Report the malaria status.
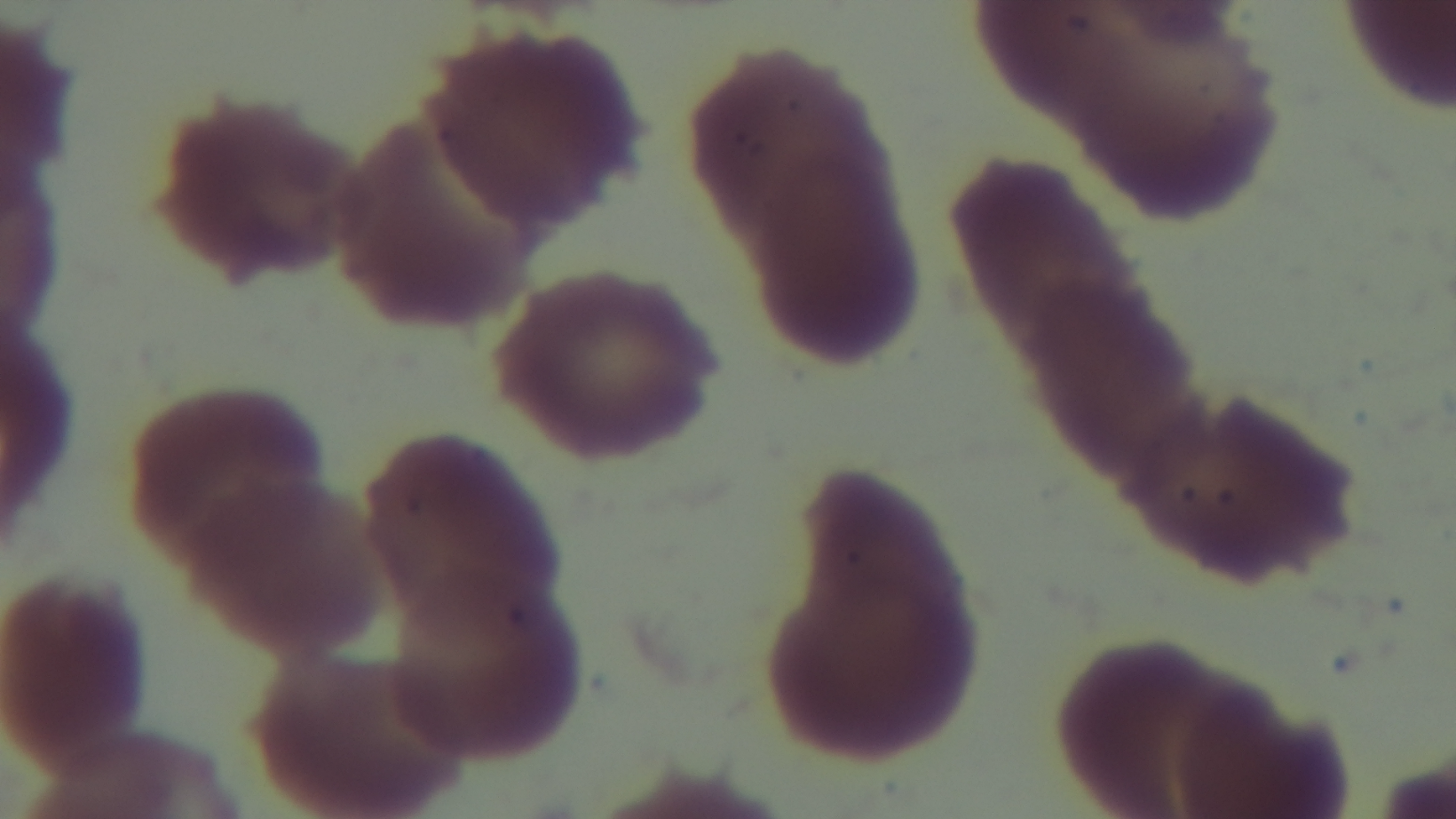
Negative.

objective = 100x oil immersion
preparation = thin
field of view = single
modality = light microscopy
stain = Giemsa
capture = mounted 4K digital camera